Locate every Plasmodium vivax-infected red blood cell.
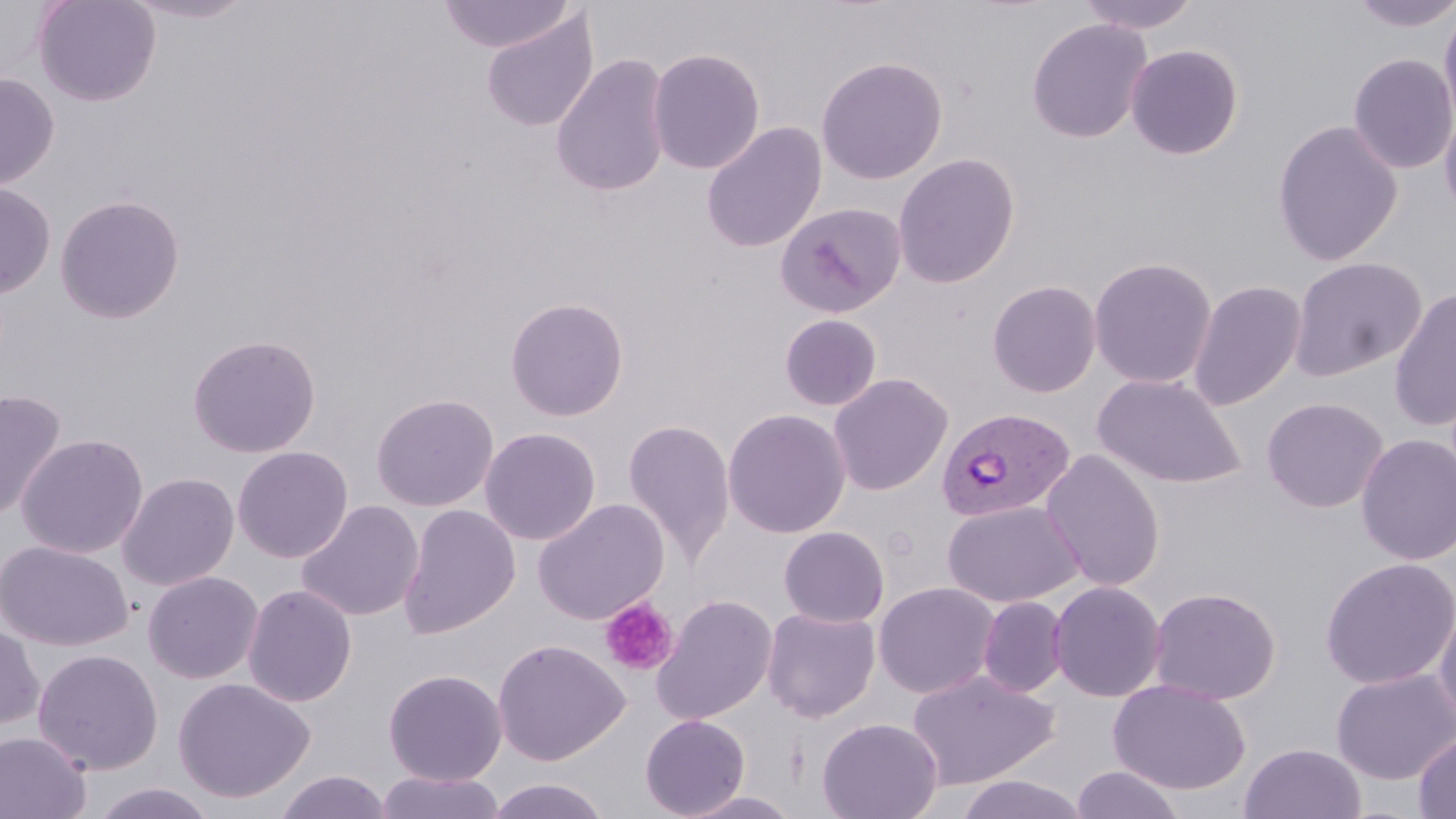

Approximate bounding boxes as (x1, y1, x2, y2) in pixels.
Plasmodium vivax-infected red blood cells: (937, 406, 1076, 522).

Summary:
  - Uninfected red blood cell locations: (33, 0, 161, 107), (121, 0, 257, 24), (437, 0, 577, 54), (1075, 0, 1202, 33), (1348, 0, 1456, 32), (1439, 4, 1456, 135), (480, 10, 600, 132), (1027, 18, 1151, 143), (1125, 44, 1243, 160), (647, 47, 765, 175), (1348, 53, 1456, 174), (551, 54, 671, 198), (816, 56, 948, 184), (0, 72, 59, 191), (1439, 103, 1456, 223), (1273, 120, 1403, 266), (701, 122, 826, 253), (893, 153, 1020, 288), (0, 182, 57, 298), (55, 194, 185, 324), (775, 201, 906, 318), (1088, 256, 1217, 388), (1288, 256, 1427, 381), (987, 279, 1102, 397), (1188, 279, 1306, 410), (1388, 288, 1456, 432), (505, 297, 629, 421), (779, 314, 882, 411), (186, 333, 322, 458), (829, 373, 953, 496), (1092, 373, 1246, 488), (0, 389, 67, 522), (371, 393, 498, 512), (1262, 396, 1388, 513), (723, 408, 850, 539), (623, 418, 735, 567), (480, 427, 601, 545), (16, 433, 148, 559), (1355, 434, 1456, 565), (232, 445, 354, 563), (1041, 449, 1165, 592), (117, 472, 239, 591), (532, 498, 670, 625), (296, 499, 424, 622), (943, 500, 1083, 608), (398, 504, 520, 639), (779, 525, 889, 628), (0, 540, 133, 652), (1320, 557, 1456, 689), (143, 571, 263, 684), (1048, 580, 1166, 702), (873, 581, 998, 699), (243, 584, 357, 707), (1148, 586, 1281, 705), (652, 594, 778, 725), (978, 596, 1068, 698), (1433, 602, 1456, 731), (761, 607, 880, 722), (0, 622, 44, 732), (493, 638, 629, 765), (32, 648, 163, 776), (383, 668, 507, 786), (1331, 668, 1456, 784), (907, 669, 1059, 790), (173, 676, 314, 804), (1108, 679, 1250, 795), (640, 714, 750, 818), (817, 716, 943, 819), (1414, 730, 1456, 819), (0, 731, 91, 819), (1240, 743, 1367, 819), (1071, 766, 1185, 818), (274, 770, 394, 819), (376, 771, 506, 819), (954, 774, 1091, 819), (485, 777, 610, 819), (89, 782, 218, 819), (679, 791, 802, 819)
  - Platelet locations: (599, 597, 678, 677)
  - Slide-level diagnosis: Plasmodium vivax
  - Preparation: thin blood film
  - Stain: May-Grünwald-Giemsa
  - Field of view: single
  - Image size: 1456×819 pixels
  - Magnification: 1000x
  - Modality: optical microscopy